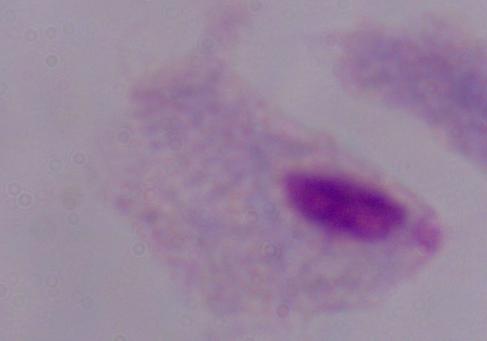 Photomicrograph. A trichomonad is seen. Captured at 1000x magnification.